Identify the cell.
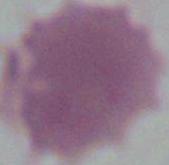
This is an erythrocyte.

{
  "modality": "photomicrograph",
  "magnification": "1000x"
}